Identify the preparation type.
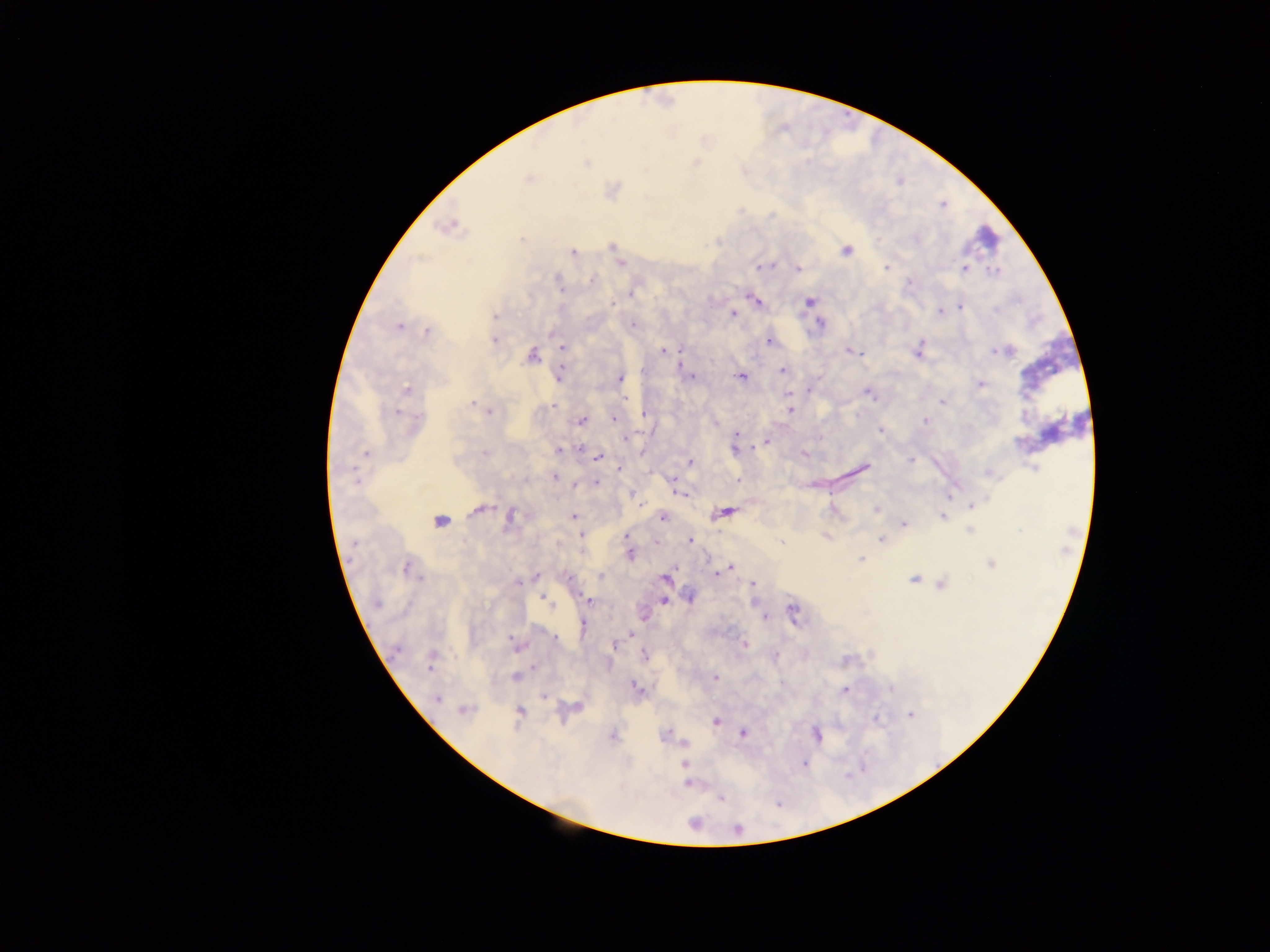
This is a thick smear.

{
  "leukocyte_locations": "approximate centers as x y in pixels: 989 233",
  "capture": "mobile-phone photograph through a microscope",
  "field_of_view": "single",
  "country": "Ghana",
  "image_size": "1270×952 pixels",
  "plasmodium_parasite_locations": "approximate centers as x y in pixels: 586 163; 528 178; 449 225; 522 239; 612 246; 846 250; 573 252; 621 264; 759 267; 886 267; 799 269; 964 269; 994 271; 590 279; 910 283; 559 285; 631 294; 755 300; 612 302; 809 302; 960 306; 939 312; 734 315; 494 316; 633 324; 820 324; 398 327; 427 332; 494 340; 769 342; 562 348; 849 350; 918 350; 996 350; 662 351; 678 353; 858 353; 531 356; 562 363; 560 371; 643 371; 782 371; 741 376; 691 377; 621 379; 981 383; 406 389; 808 390; 867 393; 789 394; 624 398; 942 402; 472 405; 553 405; 489 411; 790 411; 397 413; 645 414; 613 419; 582 420; 925 420; 881 431; 736 436; 626 438; 766 442; 580 449; 735 450; 559 451; 366 453; 485 453; 804 454; 598 457; 911 460; 690 462; 863 467; 618 469; 555 477; 673 480; 738 480; 596 482; 575 485; 676 491; 950 495; 640 505; 973 506; 481 509; 876 509; 727 512; 511 517; 573 517; 663 517; 943 517; 440 522; 904 524; 970 530; 582 536; 626 537; 881 539; 690 540; 780 542; 629 555; 861 559; 991 564; 730 567; 406 568; 717 574; 536 576; 601 576; 418 578; 665 578; 914 579; 518 583; 753 584; 941 586; 689 597; 543 599; 589 601; 664 601; 377 604; 793 612; 764 617; 583 625; 630 635; 555 638; 512 641; 745 644; 613 645; 396 651; 644 655; 775 656; 534 667; 430 668; 716 677; 515 678; 637 687; 890 689; 844 690; 543 697; 437 698; 465 710; 520 711; 910 715; 876 719; 716 722; 666 733; 743 733; 816 735; 685 744; 684 763; 804 763; 687 784; 721 798; 737 829"
}